Locate every uninfected red blood cell.
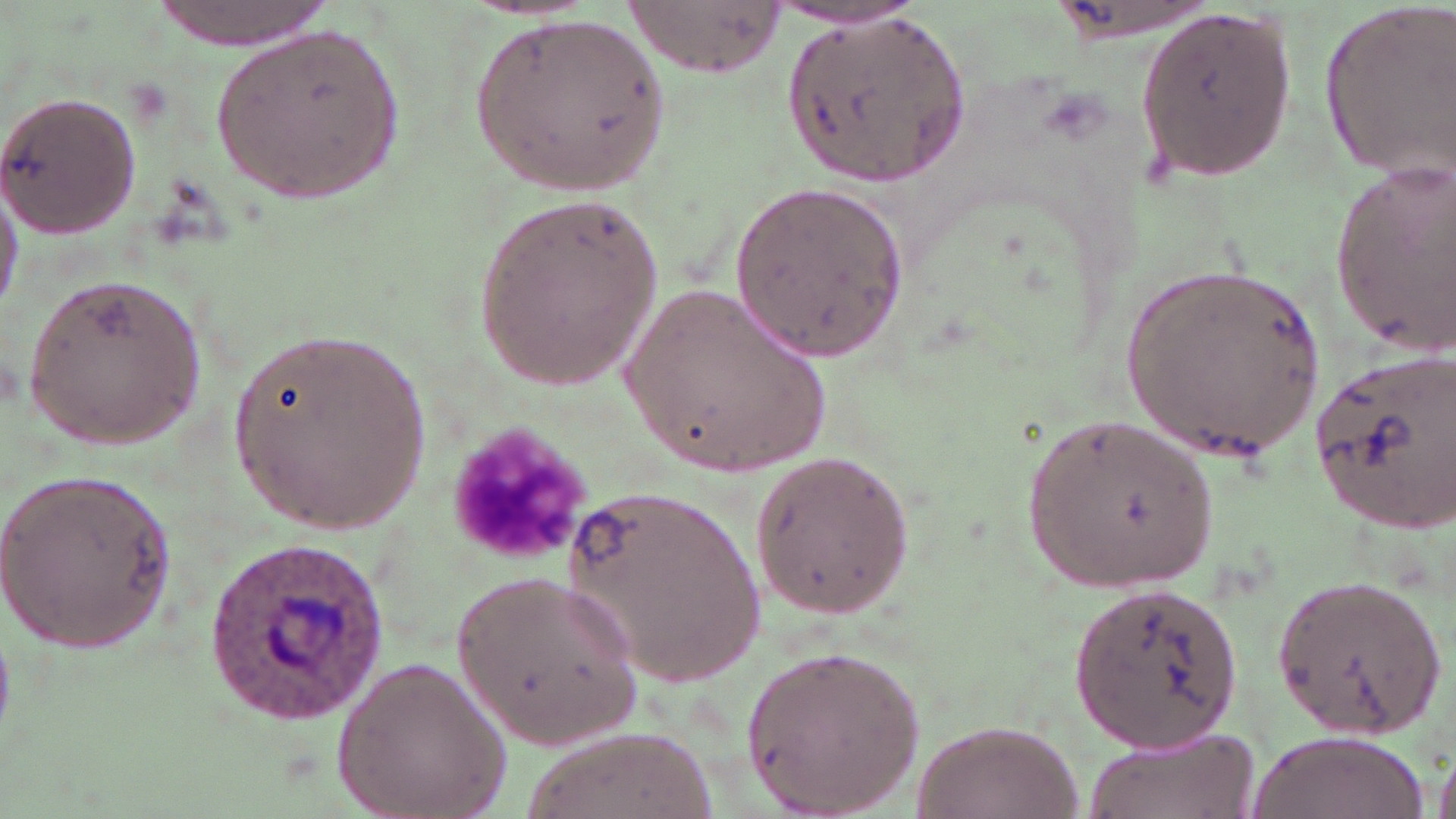

Approximate bounding boxes as (x1,y1)-(x2,y2) corner pairs in pixels.
Uninfected red blood cells: (623,0)-(782,76), (1318,1)-(1456,177), (769,3)-(926,31), (1135,5)-(1295,186), (468,11)-(671,198), (783,11)-(970,187), (210,24)-(405,207), (0,91)-(142,240), (1327,159)-(1456,359), (0,177)-(21,322), (730,181)-(909,361), (473,191)-(667,391), (1119,264)-(1330,462), (22,270)-(211,450), (622,283)-(833,481), (226,325)-(436,538), (1307,347)-(1456,531), (1027,419)-(1216,588), (747,450)-(917,618), (0,468)-(179,652), (562,482)-(769,692), (456,567)-(643,750), (1270,569)-(1447,739), (1069,580)-(1244,752), (739,644)-(926,817), (332,655)-(511,819), (903,718)-(1086,819), (1082,725)-(1259,819), (524,727)-(716,819), (1245,730)-(1427,819), (1431,741)-(1456,819).

slide-level diagnosis = Plasmodium ovale
magnification = 1000x
modality = light microscopy
platelet locations = approximate bounding boxes as (x1,y1)-(x2,y2) corner pairs in pixels: (450,426)-(586,566)
preparation = thin blood smear
image size = 1456×819 pixels
stain = May-Grünwald-Giemsa
Plasmodium ovale-infected red blood cell locations = approximate bounding boxes as (x1,y1)-(x2,y2) corner pairs in pixels: (203,541)-(400,721)
field of view = single